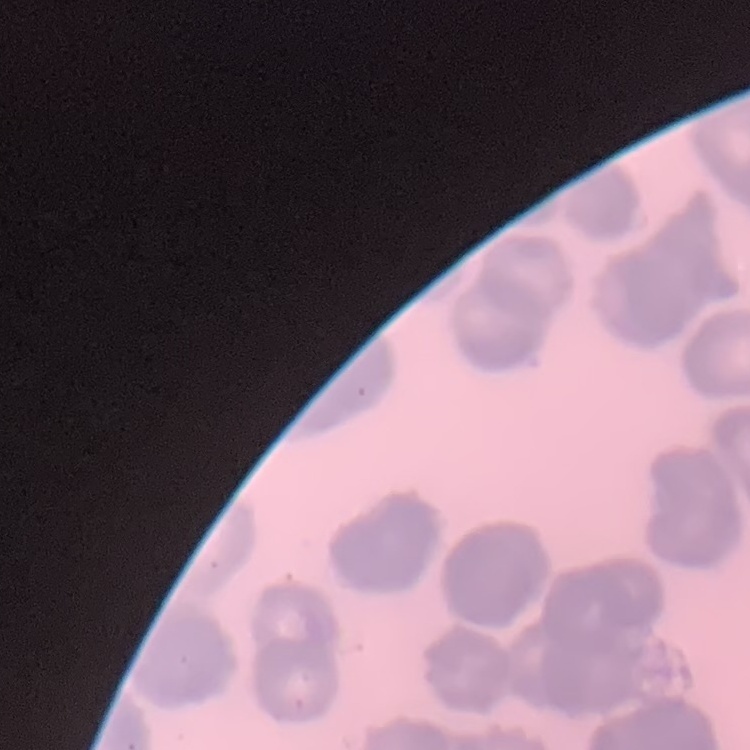 The erythrocytes show rouleaux formation. One tile cut from a larger photomicrograph. Field's or Giemsa stain. Thin blood smear.